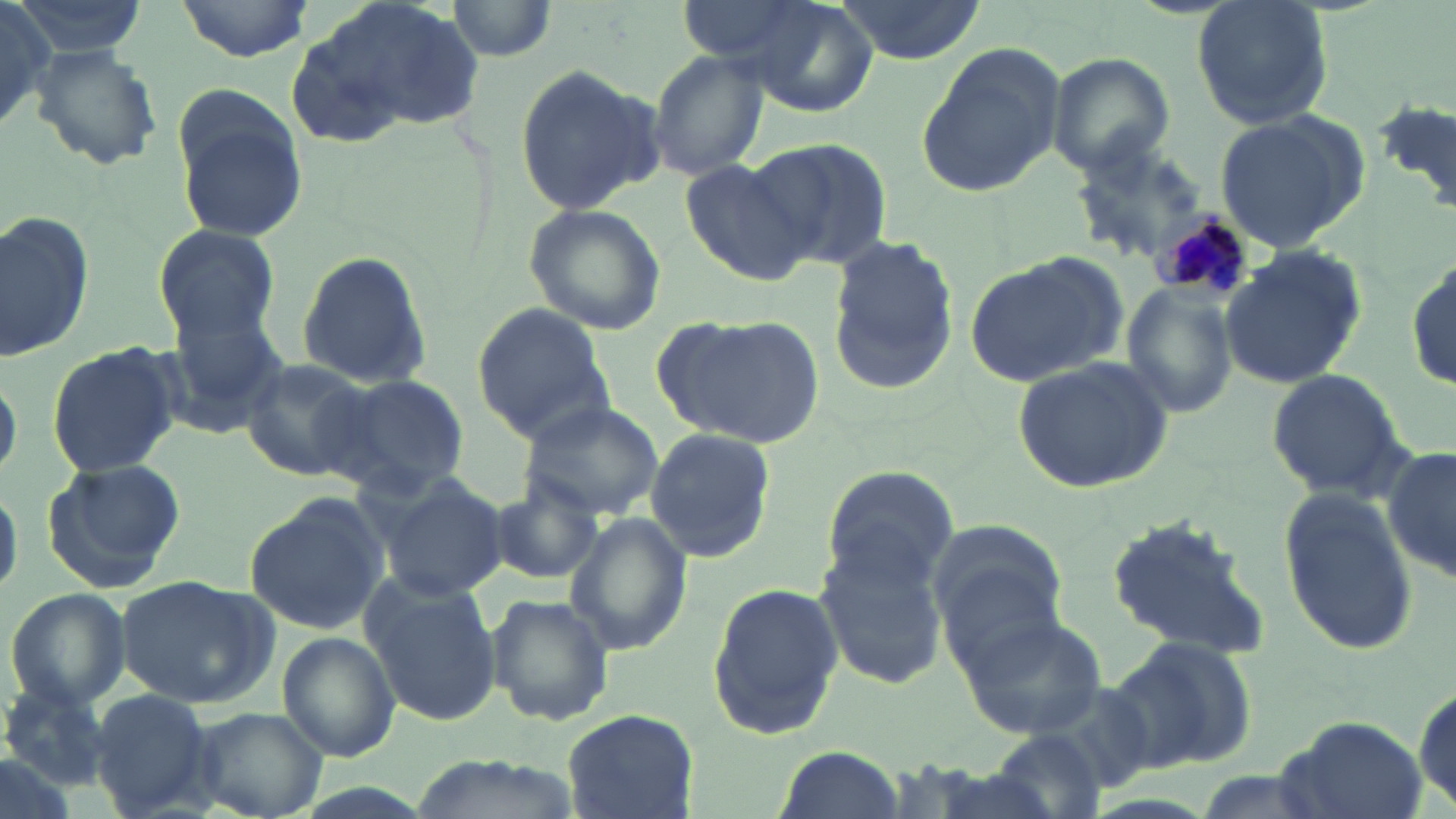

Summary:
  - Coordinate format: approximate bounding boxes as (x1,y1)-(x2,y2) corner pairs in pixels
  - Plasmodium malariae-infected red blood cell locations: (1149,208)-(1253,305)
  - Uninfected red blood cell locations: (0,0)-(62,135), (175,0)-(313,62), (286,0)-(488,148), (446,0)-(561,62), (720,0)-(881,115), (1192,0)-(1333,131), (9,1)-(149,56), (831,1)-(987,63), (32,42)-(162,172), (913,46)-(1067,197), (644,51)-(769,180), (1050,55)-(1174,176), (513,62)-(664,217), (1374,100)-(1456,219), (174,102)-(305,242), (1212,110)-(1368,252), (750,135)-(893,272), (1069,142)-(1212,261), (679,157)-(818,286), (520,201)-(667,337), (0,208)-(94,363), (152,224)-(282,345), (830,244)-(956,396), (294,248)-(432,388), (1221,248)-(1366,392), (963,257)-(1120,391), (1407,258)-(1454,393), (1122,285)-(1238,417), (471,302)-(613,443), (162,305)-(290,434), (664,313)-(824,449), (45,343)-(179,479), (238,355)-(376,483), (1010,355)-(1176,495), (0,367)-(20,484), (1264,369)-(1414,503), (334,374)-(471,496), (518,397)-(665,518), (647,428)-(774,563), (1382,447)-(1456,584), (42,458)-(184,592), (818,465)-(959,592), (375,475)-(509,601), (0,478)-(20,600), (487,480)-(605,585), (1280,491)-(1421,655), (242,493)-(387,637), (1107,513)-(1270,663), (564,515)-(694,657), (927,517)-(1070,666), (816,543)-(950,686), (117,575)-(274,708), (361,578)-(501,727), (706,582)-(843,736), (5,587)-(130,710), (486,594)-(613,726), (955,610)-(1105,738), (277,632)-(401,764), (1106,636)-(1257,773), (1411,683)-(1454,813), (2,685)-(111,788), (87,687)-(217,818), (186,707)-(327,819), (561,707)-(695,818), (1275,715)-(1432,819), (988,728)-(1107,819), (770,744)-(906,819), (0,752)-(80,819), (915,767)-(1072,819)
  - Slide-level diagnosis: Plasmodium malariae
  - Magnification: 1000x
  - Image size: 1456×819 pixels
  - Preparation: thin blood film
  - Field of view: single
  - Modality: optical microscopy
  - Stain: May-Grünwald-Giemsa